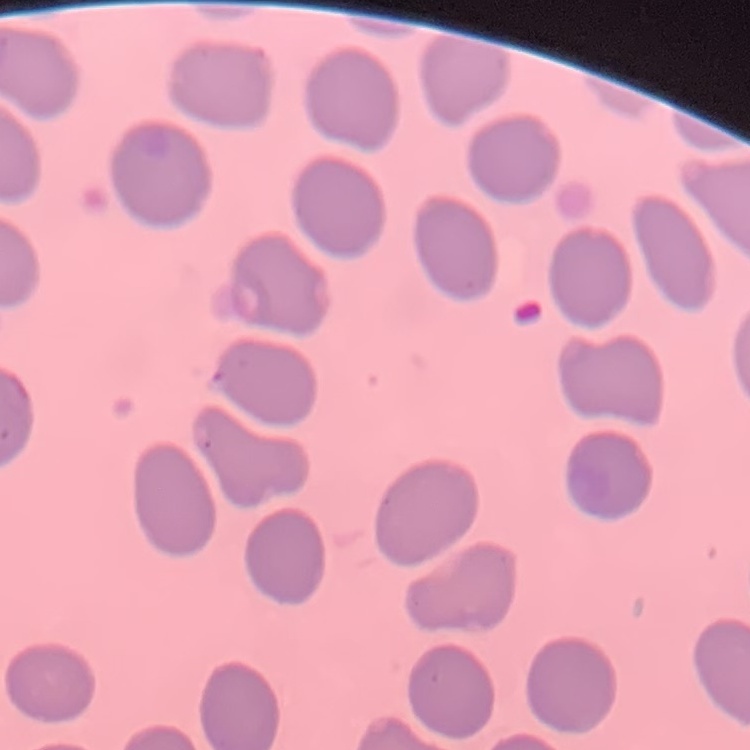

red blood cell morphology = no rouleaux formation
stain = Field's or Giemsa
image type = square crop of a larger photomicrograph
preparation = thin peripheral smear